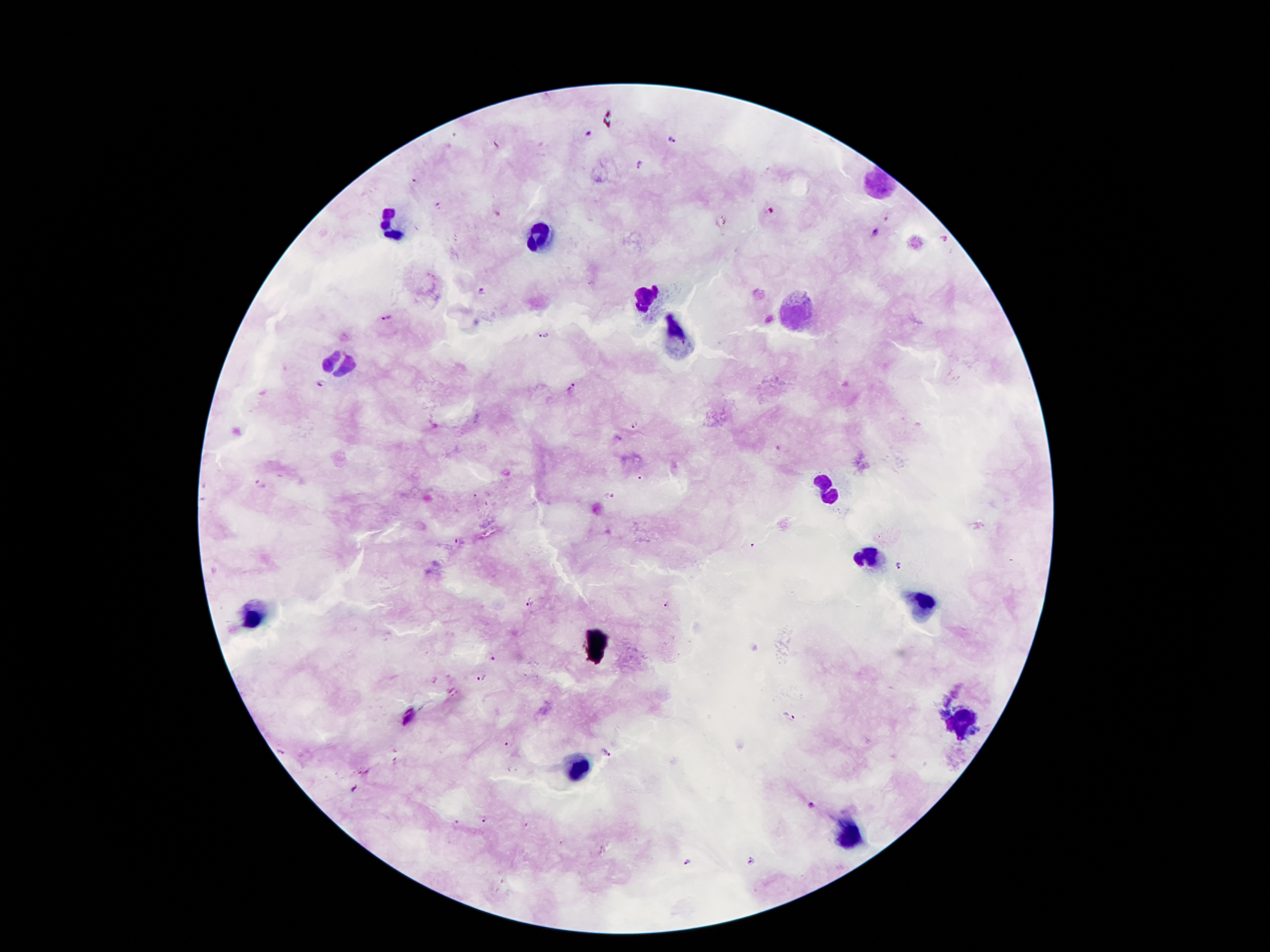 Giemsa stain. Photographed through the microscope eyepiece with a smartphone camera. One field from this slide. Patient malaria status: infected with Plasmodium falciparum. 100x magnification. Image is 1270×952 pixels. Thick peripheral-blood smear.